Give the extent of all Plasmodium falciparum-infected red blood cells.
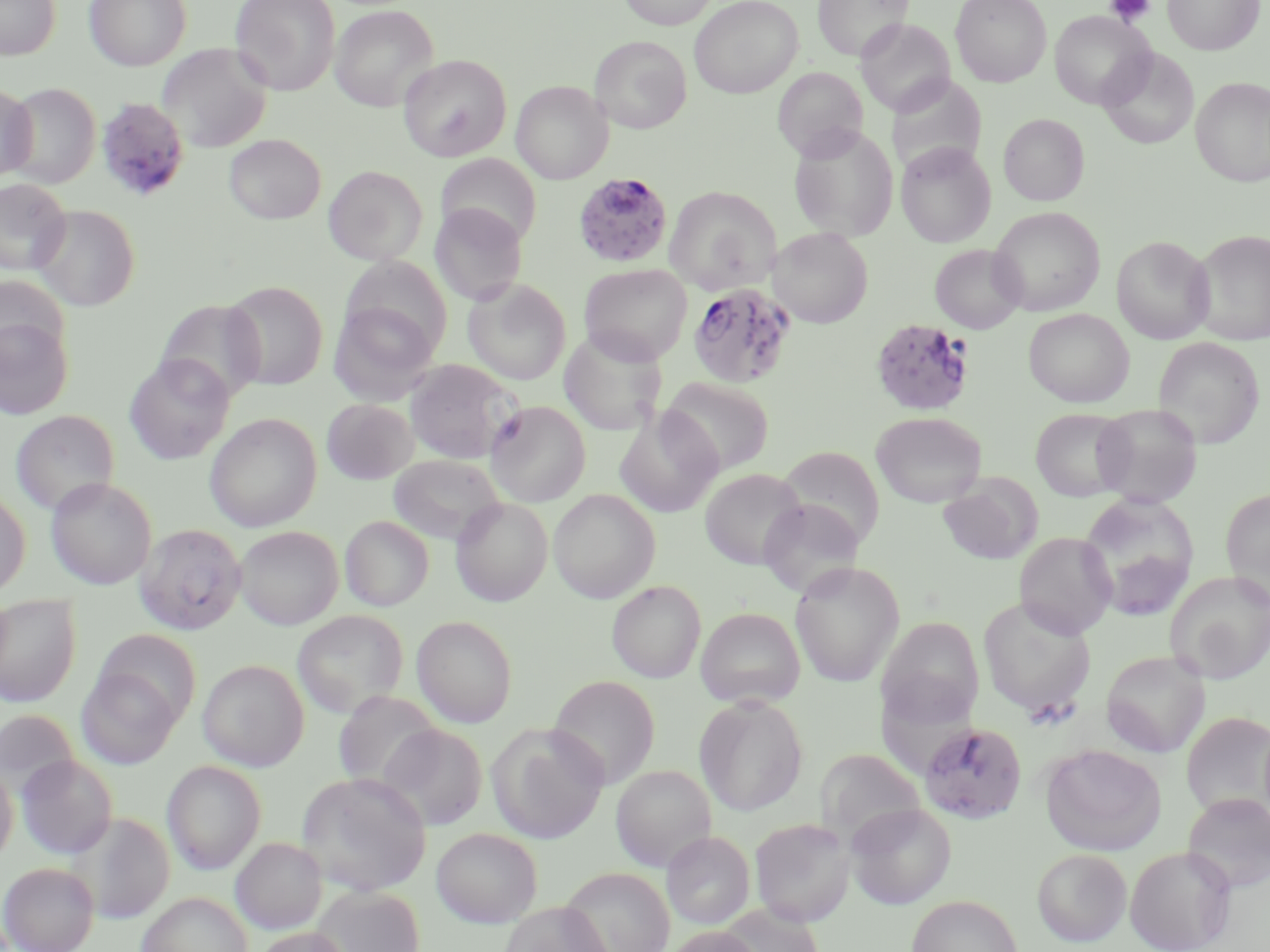
Approximate bounding boxes as [x1, y1, x2, y2] in pixels.
Plasmodium falciparum-infected red blood cells: [96, 97, 190, 202], [573, 171, 674, 268], [687, 280, 797, 389], [869, 317, 976, 417], [919, 721, 1028, 824].

Summary:
  - Platelet locations: [1105, 0, 1156, 25]
  - Uninfected red blood cell locations: [0, 0, 61, 60], [84, 0, 191, 71], [230, 0, 340, 96], [618, 0, 718, 29], [689, 0, 802, 98], [814, 0, 913, 61], [950, 0, 1051, 87], [1162, 0, 1263, 55], [330, 5, 438, 111], [1049, 11, 1153, 110], [856, 18, 955, 117], [590, 36, 692, 133], [157, 43, 273, 153], [1099, 47, 1199, 149], [399, 54, 512, 161], [772, 67, 868, 160], [886, 75, 987, 176], [1191, 77, 1270, 186], [511, 80, 612, 183], [0, 83, 37, 181], [5, 83, 101, 189], [999, 113, 1089, 206], [788, 124, 899, 241], [224, 134, 325, 224], [896, 141, 996, 247], [436, 154, 542, 248], [324, 165, 427, 265], [0, 179, 71, 275], [665, 185, 781, 294], [430, 203, 527, 306], [31, 205, 140, 312], [989, 206, 1106, 316], [770, 227, 873, 328], [1189, 229, 1270, 346], [1111, 235, 1215, 344], [930, 244, 1025, 334], [340, 257, 454, 359], [579, 263, 692, 365], [0, 275, 69, 365], [464, 279, 571, 385], [223, 280, 328, 390], [328, 301, 440, 404], [1024, 308, 1134, 407], [0, 317, 73, 419], [558, 328, 668, 436], [1153, 337, 1264, 448], [124, 355, 234, 464], [404, 359, 520, 463], [661, 377, 774, 477], [321, 398, 416, 484], [485, 401, 591, 506], [1091, 404, 1203, 508], [615, 407, 723, 518], [1031, 408, 1132, 501], [11, 410, 119, 516], [871, 411, 987, 507], [205, 413, 322, 532], [779, 445, 886, 547], [388, 454, 506, 547], [699, 469, 806, 569], [938, 474, 1041, 565], [46, 477, 157, 590], [1220, 488, 1270, 606], [0, 489, 30, 597], [548, 489, 660, 603], [1078, 492, 1200, 621], [451, 497, 553, 606], [758, 498, 863, 599], [340, 516, 433, 611], [134, 523, 247, 635], [234, 526, 343, 629], [1014, 531, 1117, 638], [790, 561, 905, 687], [1166, 571, 1270, 684], [607, 580, 706, 683], [0, 595, 81, 707], [977, 598, 1096, 718], [695, 607, 805, 708], [293, 611, 408, 719], [412, 614, 517, 727], [878, 616, 985, 724], [95, 629, 202, 725], [1101, 650, 1210, 757], [198, 659, 308, 771], [76, 668, 181, 769], [548, 675, 660, 789], [334, 690, 442, 792], [694, 695, 809, 816], [0, 708, 81, 801], [1181, 711, 1270, 820], [379, 723, 487, 831], [487, 723, 608, 844], [1040, 743, 1167, 856], [814, 747, 926, 842], [16, 754, 118, 859], [162, 760, 266, 875], [0, 762, 18, 865], [611, 765, 716, 871], [296, 771, 431, 897], [1182, 792, 1270, 893], [845, 803, 956, 909], [68, 811, 175, 923], [749, 818, 856, 927], [431, 827, 543, 928], [662, 831, 755, 929], [231, 837, 327, 934], [1125, 845, 1237, 952], [1032, 848, 1132, 946], [1, 862, 98, 952], [559, 867, 675, 952], [311, 885, 424, 952], [137, 891, 252, 952], [906, 895, 1023, 952], [498, 901, 613, 952], [716, 902, 824, 952], [664, 926, 764, 952], [251, 927, 353, 952]
  - Slide-level diagnosis: Plasmodium falciparum
  - Preparation: thin blood smear
  - Modality: light microscopy
  - Field of view: one of a larger specimen
  - Stain: May-Grünwald-Giemsa
  - Image size: 1270×952 pixels
  - Magnification: 1000x